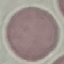

Summary:
  - Malaria status: uninfected
  - Stain: Giemsa
  - Preparation: thin blood film
  - Capture: smartphone through the microscope eyepiece
  - Image type: automatically extracted cell patch, resized to 64 × 64 pixels